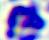

modality = micrograph
identification = white blood cell
magnification = 400x